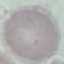
Summary:
  - Result: no malaria parasites detected
  - Preparation: thin smear
  - Capture: smartphone camera at the microscope eyepiece
  - Stain: Giemsa
  - Image type: cell patch, automatically extracted from a larger field of view and resized to 64 × 64 pixels